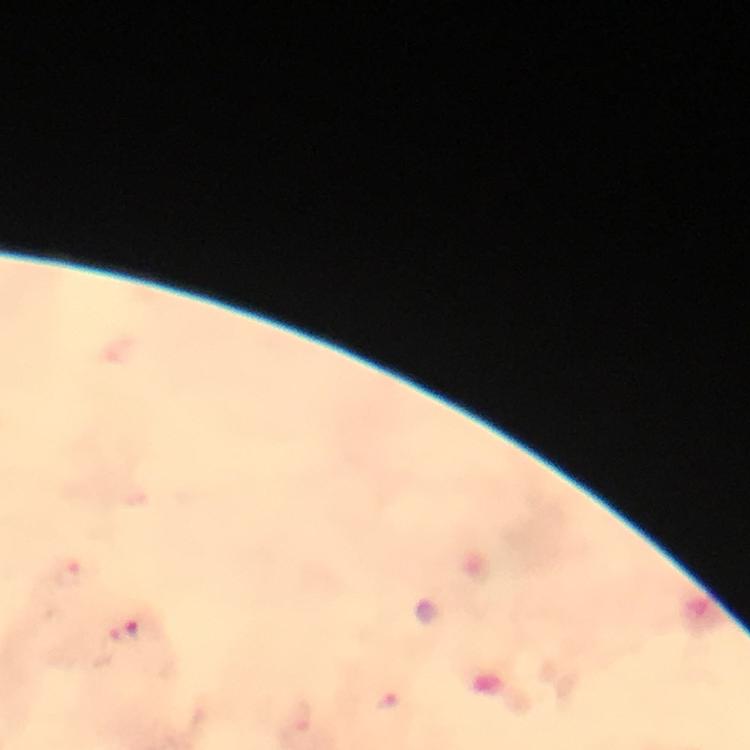
Approximate centers as [x, y] in pixels.
Summary:
  - Plasmodium parasite locations: [72, 578], [126, 633], [390, 705]
  - Cropped from: one field of view
  - Preparation: thick smear
  - Image size: 750×750 pixels
  - Immersion oil: used
  - Stain: Giemsa
  - Capture: smartphone camera through the microscope
  - Magnification: 100x
  - Context: from a diagnostic examination for malaria